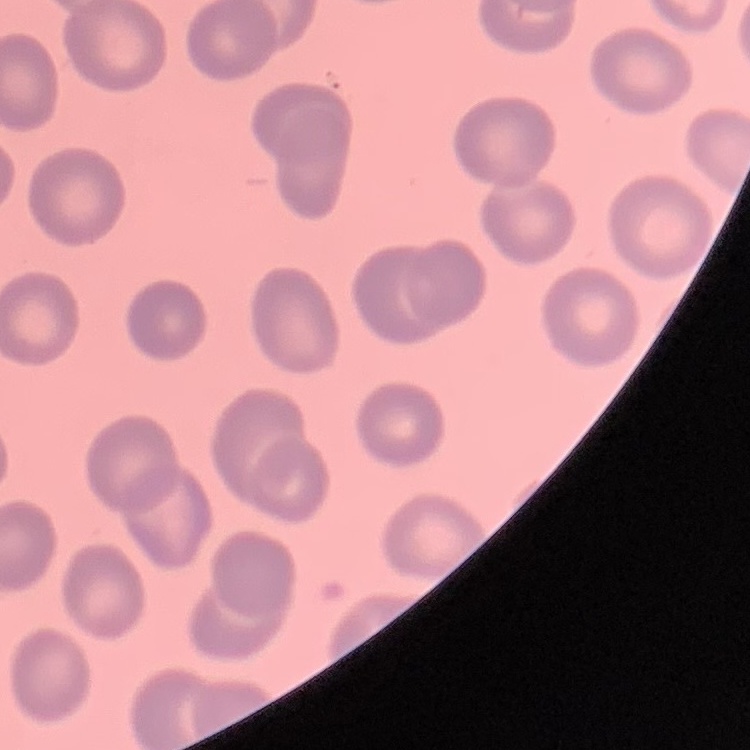
The red blood cells exhibit no rouleaux formation. One tile cut from a larger photomicrograph. Thin blood smear. Stained with either Field's or Giemsa.